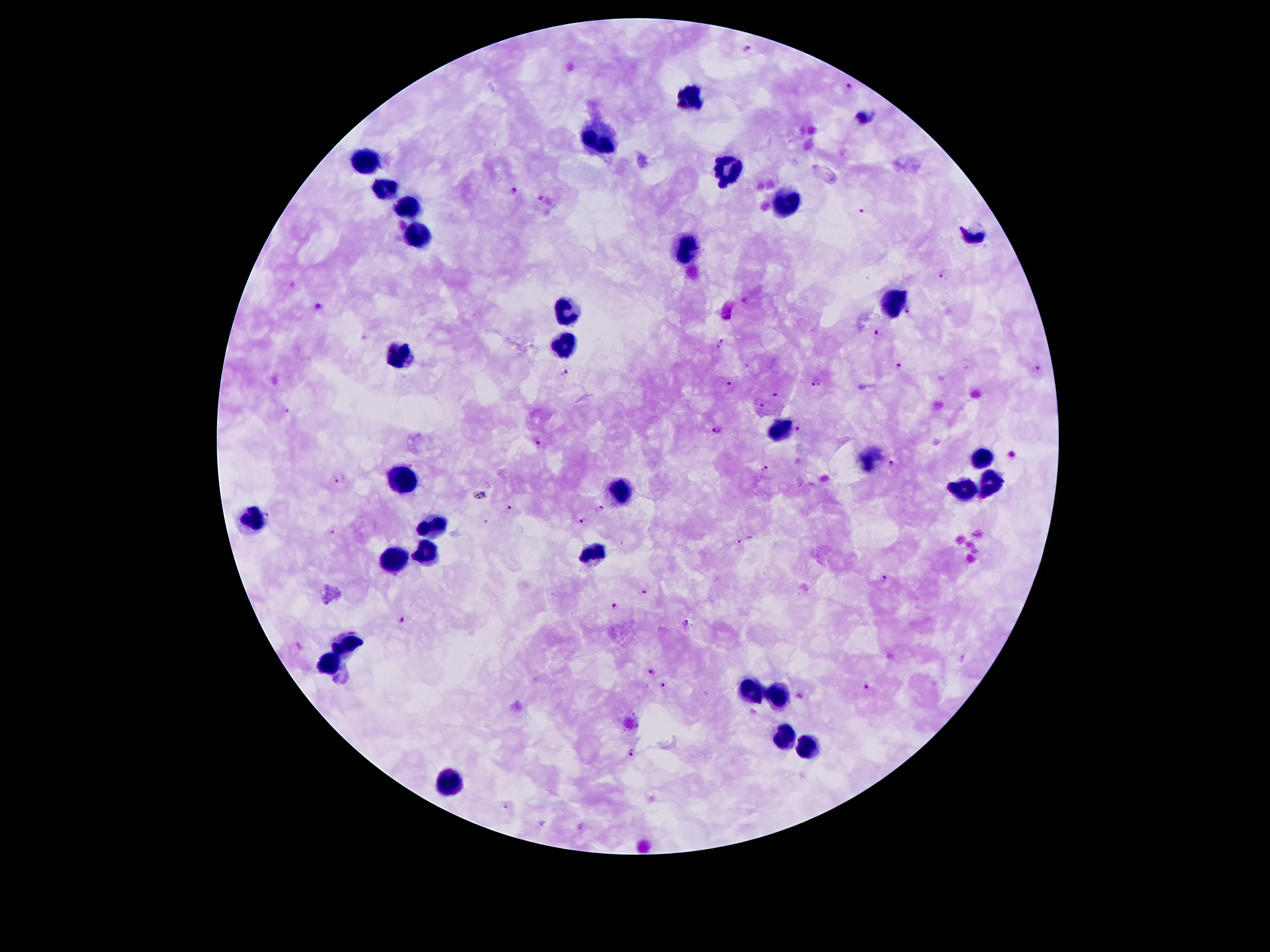
Approximate centers as [x, y] in pixels. Leukocyte locations: [690, 96], [599, 139], [366, 159], [736, 169], [383, 190], [786, 200], [407, 208], [972, 236], [417, 237], [690, 249], [894, 301], [568, 308], [562, 343], [403, 354], [779, 430], [980, 458], [406, 479], [989, 484], [965, 486], [621, 488], [252, 521], [433, 526], [423, 551], [592, 554], [392, 561], [346, 646], [329, 664], [751, 688], [779, 696], [785, 738], [806, 747], [447, 780]. Plasmodium parasite locations: [747, 50], [848, 86], [514, 190], [541, 198], [863, 208], [942, 276], [320, 305], [727, 312], [910, 312], [877, 332], [720, 343], [898, 363], [1035, 369], [565, 372], [730, 383], [816, 383], [776, 392], [759, 403], [283, 409], [716, 429], [799, 429], [538, 443], [1013, 455], [894, 466], [766, 469], [339, 476], [510, 506], [601, 510], [581, 520], [333, 531], [740, 541], [884, 578], [643, 592], [615, 604], [403, 621], [686, 624], [299, 645], [651, 672], [663, 685], [867, 685], [628, 755], [507, 807]. Thick peripheral-blood smear. One field from this slide. Smartphone photograph taken through the microscope eyepiece. 100x magnification. Patient malaria status: infected with Plasmodium falciparum. Image is 1270×952 pixels. Giemsa-stained preparation.